Look for Plasmodium parasites.
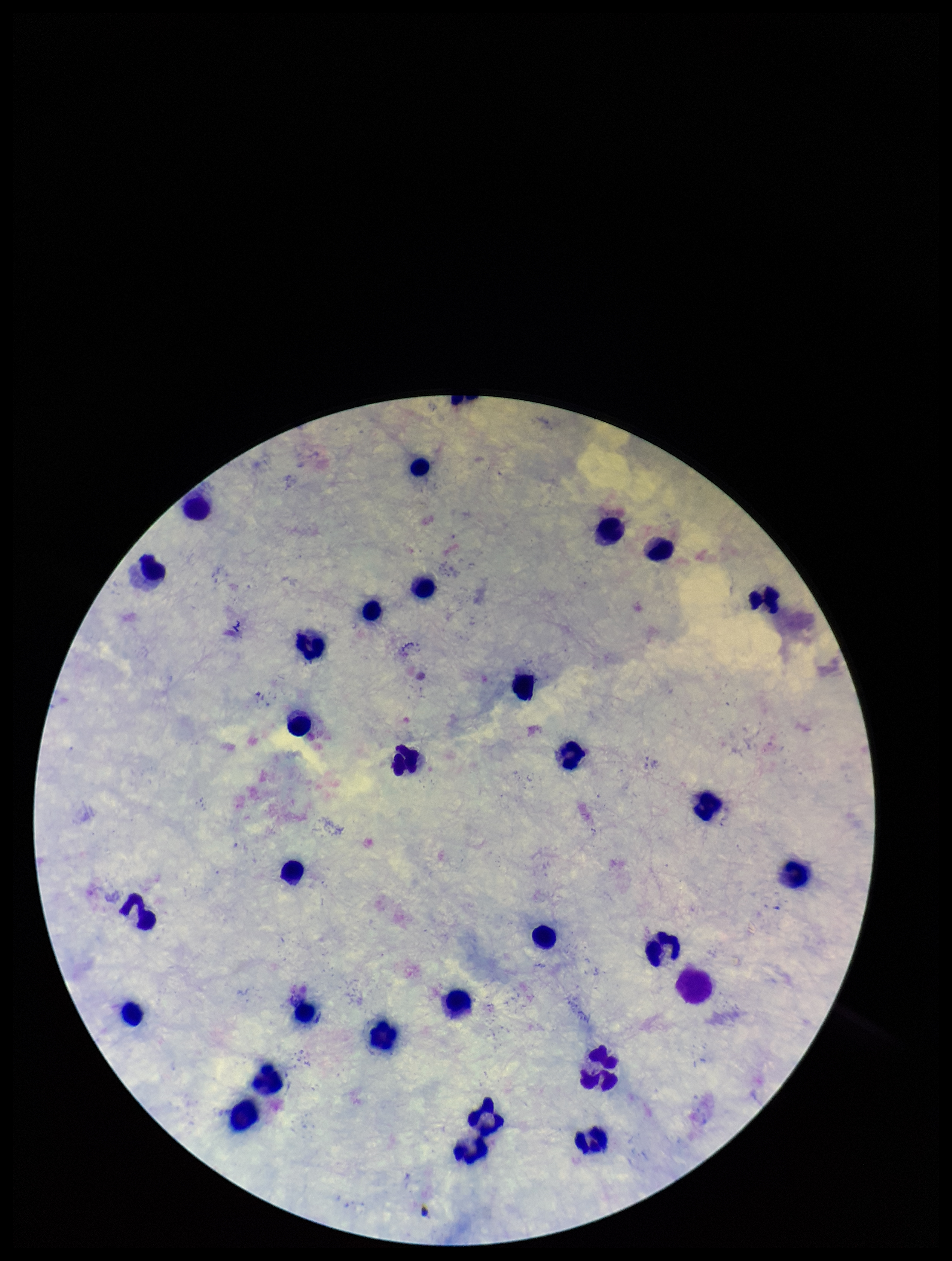
None detected.

{
  "stain": "Giemsa",
  "parasite_count": 0,
  "capture": "smartphone photograph through the microscope eyepiece",
  "patient_malaria_status": "negative",
  "field_of_view": "single",
  "preparation": "thick",
  "leukocyte_count": 30,
  "image_size": "952×1261 pixels"
}